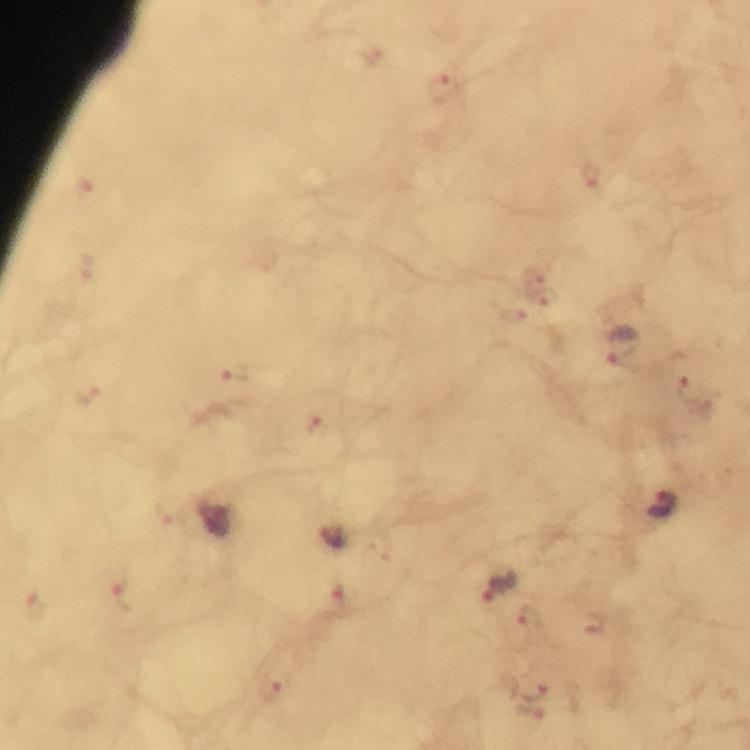
Approximate object centers, in pixels from the top-left corner. Malaria parasite locations: (x=444, y=86), (x=591, y=176), (x=83, y=190), (x=540, y=287), (x=621, y=346), (x=233, y=373), (x=693, y=394), (x=86, y=395), (x=316, y=425), (x=661, y=506), (x=331, y=536), (x=501, y=586), (x=124, y=595), (x=528, y=619), (x=595, y=624), (x=270, y=689). Immersion oil was used. Photographed with a smartphone mounted on the microscope. From a malaria diagnostic workup. Thick blood smear. A crop from one field of view. Giemsa-stained preparation. Image is 750×750 pixels. At 100x magnification.